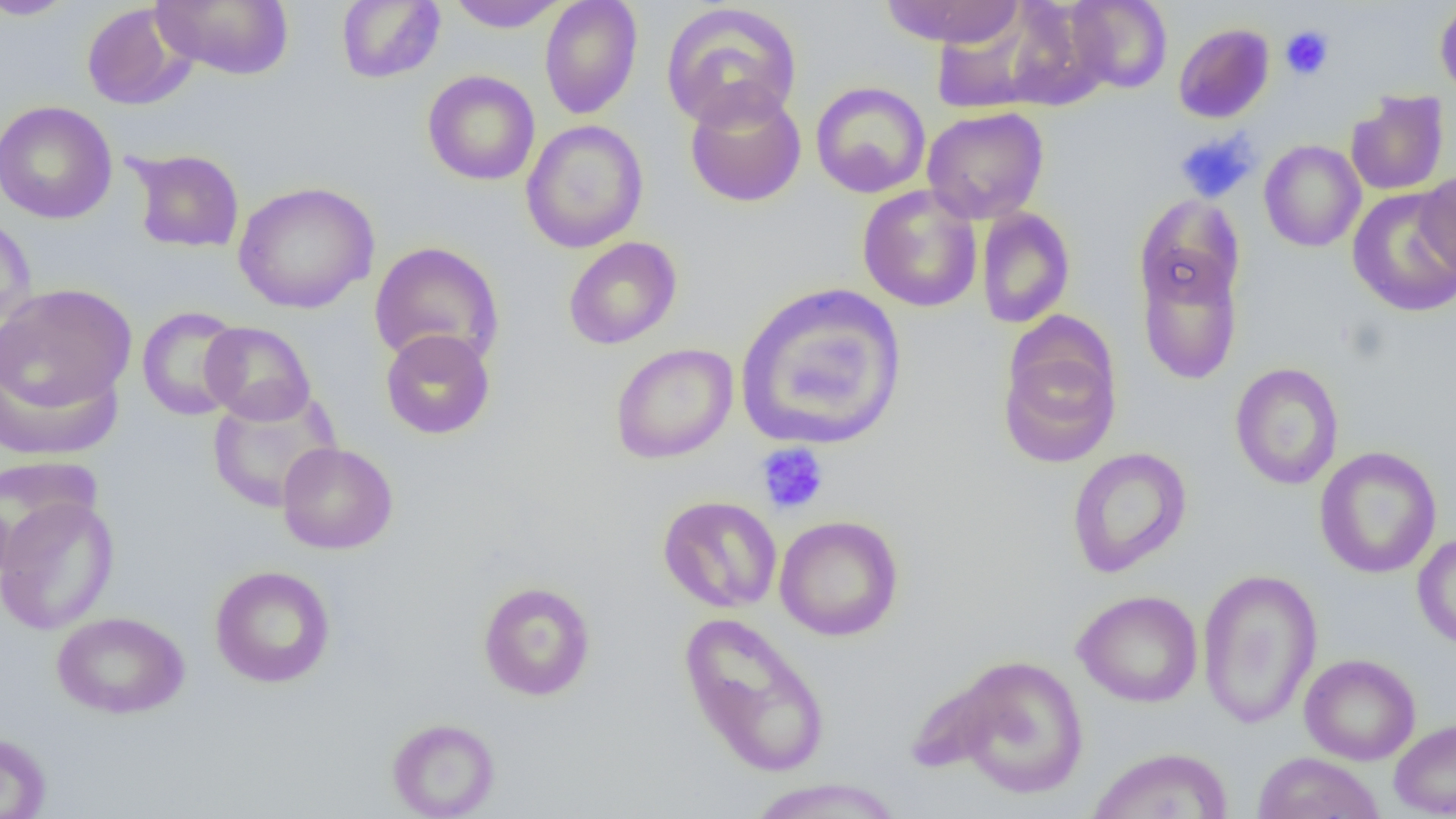

slide_level_diagnosis: negative for blood parasites
modality: optical microscopy
field_of_view: single
preparation: thin blood smear
uninfected_red_blood_cell_locations: 'approximate bounding boxes as (x1,y1)-(x2,y2) corner pairs in pixels: (0,0)-(80,20), (152,0)-(294,80), (445,0)-(569,32), (539,0)-(643,120), (879,0)-(1025,47), (1066,0)-(1172,93), (336,1)-(445,84), (1434,1)-(1456,101), (660,2)-(803,132), (81,3)-(195,110), (932,5)-(1071,117), (1173,22)-(1275,124), (422,69)-(540,186), (810,81)-(931,198), (684,84)-(807,208), (1345,91)-(1449,196), (0,100)-(117,224), (922,106)-(1049,224), (521,120)-(648,253), (1258,139)-(1366,252), (127,148)-(245,254), (1414,171)-(1456,280), (233,181)-(379,314), (857,185)-(983,312), (1347,188)-(1456,317), (1135,194)-(1245,311), (975,207)-(1075,329), (0,212)-(38,337), (563,236)-(683,349), (369,241)-(505,369), (1137,253)-(1243,384), (735,282)-(909,452), (1,283)-(137,418), (136,306)-(247,420), (200,321)-(315,425), (380,328)-(495,439), (998,331)-(1121,469), (610,343)-(738,464), (0,351)-(124,461), (1229,362)-(1345,490), (206,389)-(342,514), (277,441)-(398,554), (1314,446)-(1442,578), (1067,447)-(1192,578), (0,456)-(99,570), (0,494)-(119,635), (658,495)-(782,613), (774,515)-(904,641), (1412,533)-(1456,650), (209,565)-(336,688), (1196,568)-(1323,729), (477,580)-(596,701), (1073,590)-(1203,707), (51,611)-(190,719), (678,611)-(831,779), (1299,653)-(1421,765), (945,654)-(1090,800), (387,717)-(501,818), (1388,717)-(1456,817), (0,731)-(52,819), (1087,746)-(1234,819), (1253,752)-(1385,818), (746,777)-(906,818)'
magnification: 1000x
platelet_locations: 'approximate bounding boxes as (x1,y1)-(x2,y2) corner pairs in pixels: (1279,25)-(1334,80), (1174,129)-(1259,203), (756,443)-(829,515)'
image_size: 1456×819 pixels